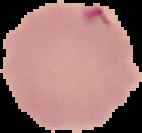

Summary:
  - Image size: 142×133 pixels
  - Image type: segmented cell region with the area outside set to black
  - Result: Plasmodium parasites identified
  - Preparation: thin blood film